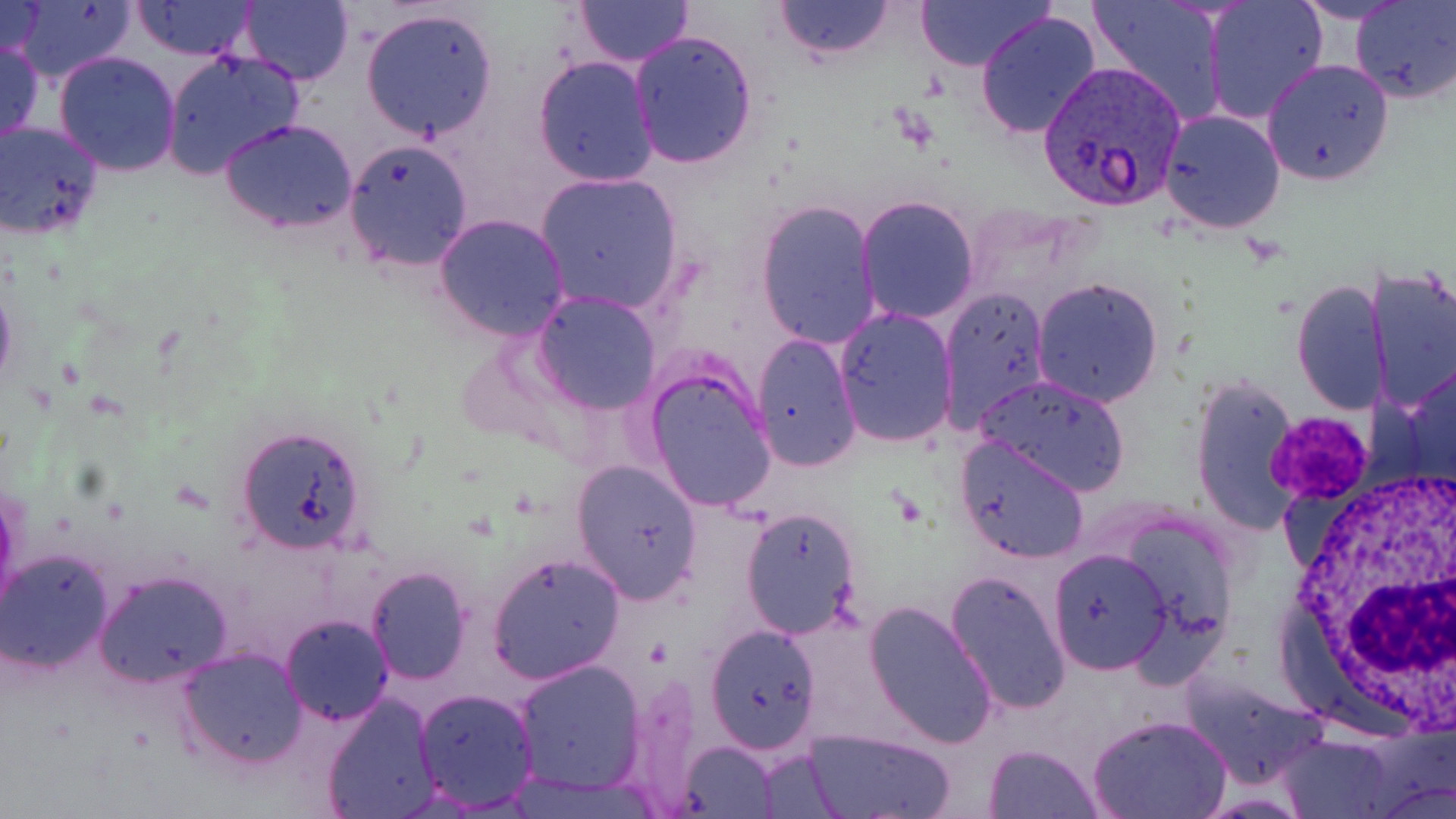 Approximate bounding boxes as (x1,y1)-(x2,y2) corner pairs in pixels. Uninfected red blood cell locations: (8,0)-(137,85), (130,0)-(257,60), (573,0)-(691,65), (774,0)-(895,59), (916,0)-(1052,71), (1086,0)-(1228,126), (1202,0)-(1329,126), (1289,0)-(1414,24), (1351,0)-(1455,104), (240,1)-(354,85), (0,2)-(47,60), (360,5)-(499,142), (976,10)-(1103,141), (628,29)-(758,171), (1,37)-(44,148), (53,50)-(182,176), (159,51)-(304,180), (533,55)-(658,187), (1263,58)-(1394,186), (1158,108)-(1287,235), (0,119)-(105,241), (220,119)-(360,234), (341,138)-(474,271), (534,171)-(684,316), (856,195)-(980,324), (756,198)-(881,351), (433,212)-(570,342), (1365,263)-(1456,414), (0,269)-(17,401), (1031,276)-(1165,408), (1292,278)-(1390,415), (940,284)-(1051,433), (533,291)-(662,414), (833,307)-(959,449), (753,333)-(861,472), (1401,356)-(1456,493), (643,361)-(778,513), (975,373)-(1132,497), (1190,376)-(1301,535), (235,424)-(369,552), (954,432)-(1091,563), (569,457)-(704,605), (0,489)-(23,625), (738,504)-(863,641), (1048,545)-(1173,675), (0,546)-(115,673), (488,553)-(625,684), (364,567)-(472,685), (94,569)-(234,688), (944,569)-(1072,716), (862,599)-(998,748), (280,614)-(393,725), (703,623)-(823,755), (179,646)-(307,770), (511,659)-(646,794), (1179,671)-(1329,788), (414,686)-(538,812), (321,694)-(441,819), (1087,714)-(1231,819), (805,728)-(956,818), (1282,734)-(1394,818), (678,740)-(780,816), (983,742)-(1102,818). Plasmodium vivax-infected red blood cell locations: (1039,64)-(1185,212). White blood cell locations: (1279,467)-(1456,724). Platelet locations: (1270,412)-(1372,504). Slide-level diagnosis: Plasmodium vivax. One field of a larger specimen. May-Grünwald-Giemsa-stained preparation. Optical microscopy. Image is 1456×819 pixels. 1000x magnification. Thin blood smear.